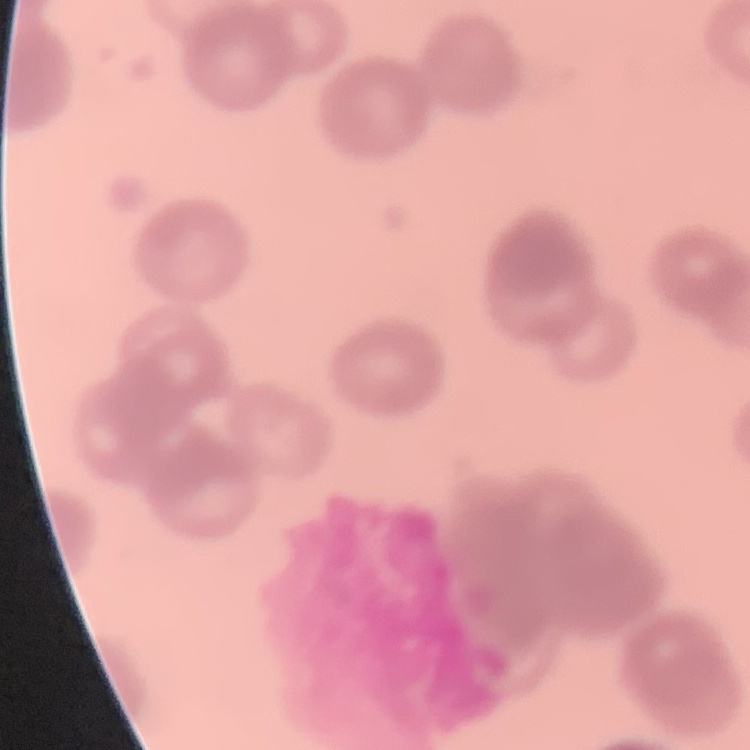 The red blood cells show rouleaux formation. Field's or Giemsa stain. Thin peripheral smear. One tile cut from a larger photomicrograph.